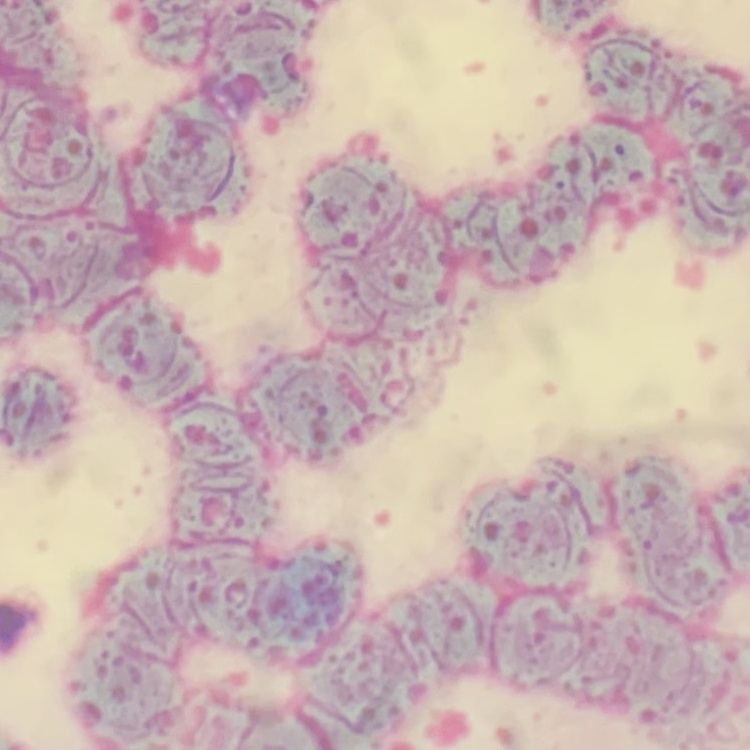

Summary:
  - Red blood cell morphology: rouleaux formation
  - Stain: Field's or Giemsa
  - Image type: square crop of a larger photomicrograph
  - Preparation: thin peripheral smear